Outline every leukocyte.
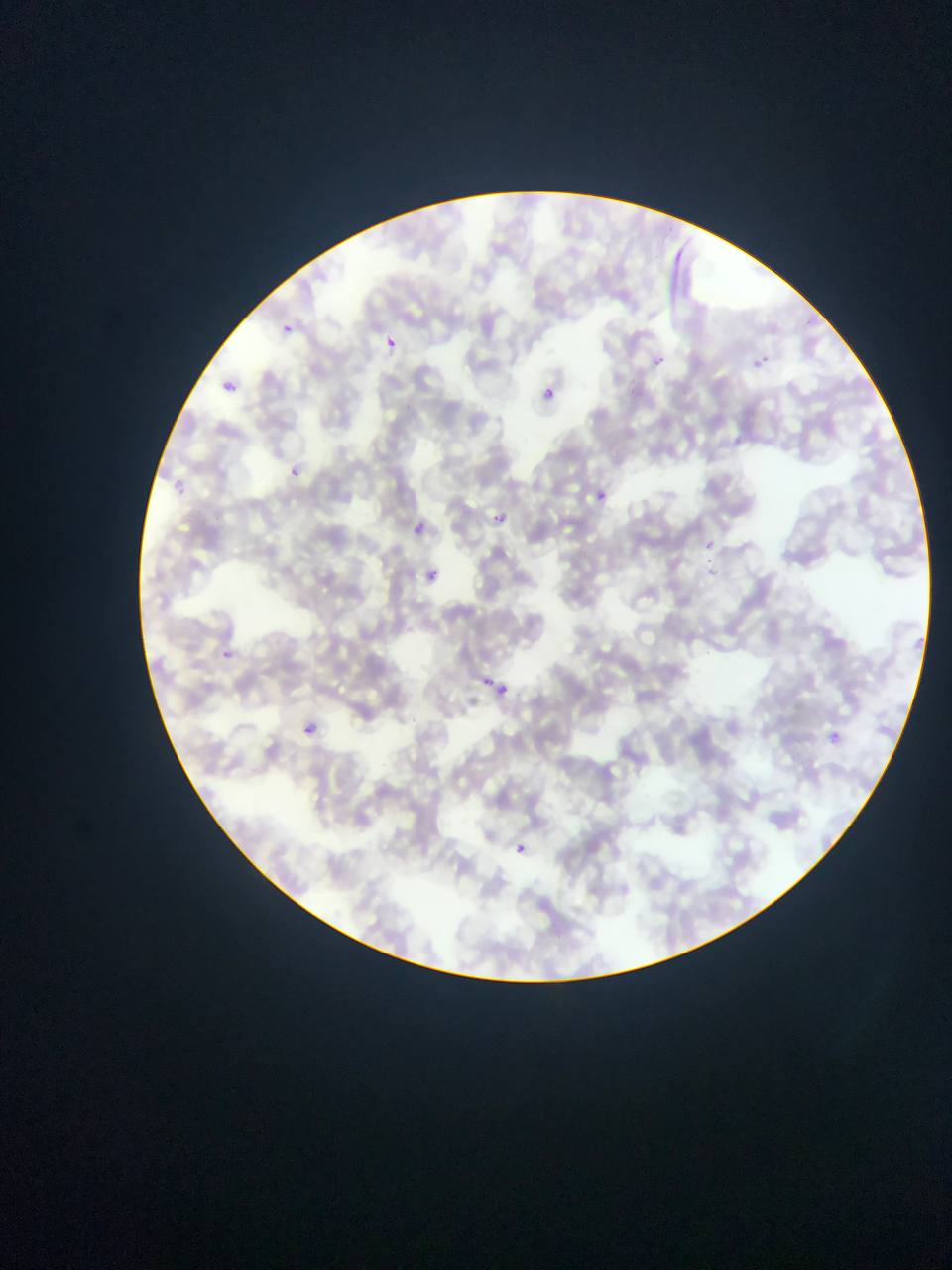

No leukocytes observed.

Approximate bounding boxes as left top right bottom in pixels.
Summary:
  - Malaria parasite locations: 797 315 828 338; 264 317 296 334; 380 331 409 349; 651 347 674 369; 752 350 773 369; 217 373 240 391; 528 381 552 396; 284 460 308 477; 171 471 195 493; 597 490 607 502; 479 495 509 525; 412 518 429 535; 706 540 714 549; 403 558 444 583; 216 639 242 660; 475 669 497 679; 490 684 508 700; 303 724 317 737; 830 731 842 742; 514 843 528 855
  - Field of view: single
  - Country: Ghana
  - Preparation: thin blood film
  - Capture: mobile-phone photograph through a microscope
  - Image size: 952×1270 pixels